Describe the morphology of the erythrocytes.
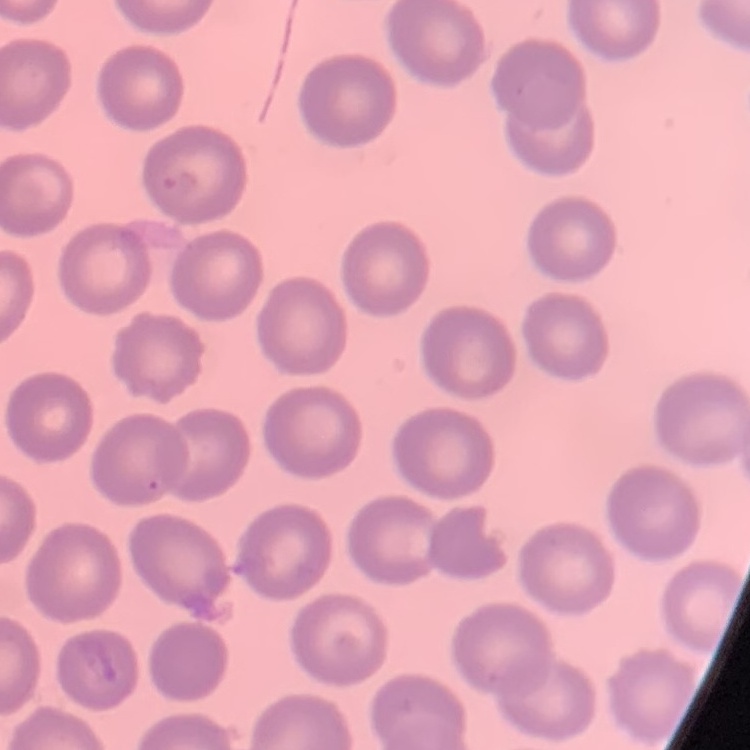

No rouleaux formation.

preparation = thin blood smear
image type = square crop of a larger photomicrograph
stain = Field's or Giemsa